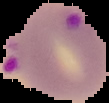 Image is 109×103 pixels. Result: malaria parasites detected. Cell region segmented out of the field of view; the surrounding area is masked to black. From a thin blood film.